Give the position of each P. falciparum parasite with its life-cycle stage, each leukocyte, and any debris.
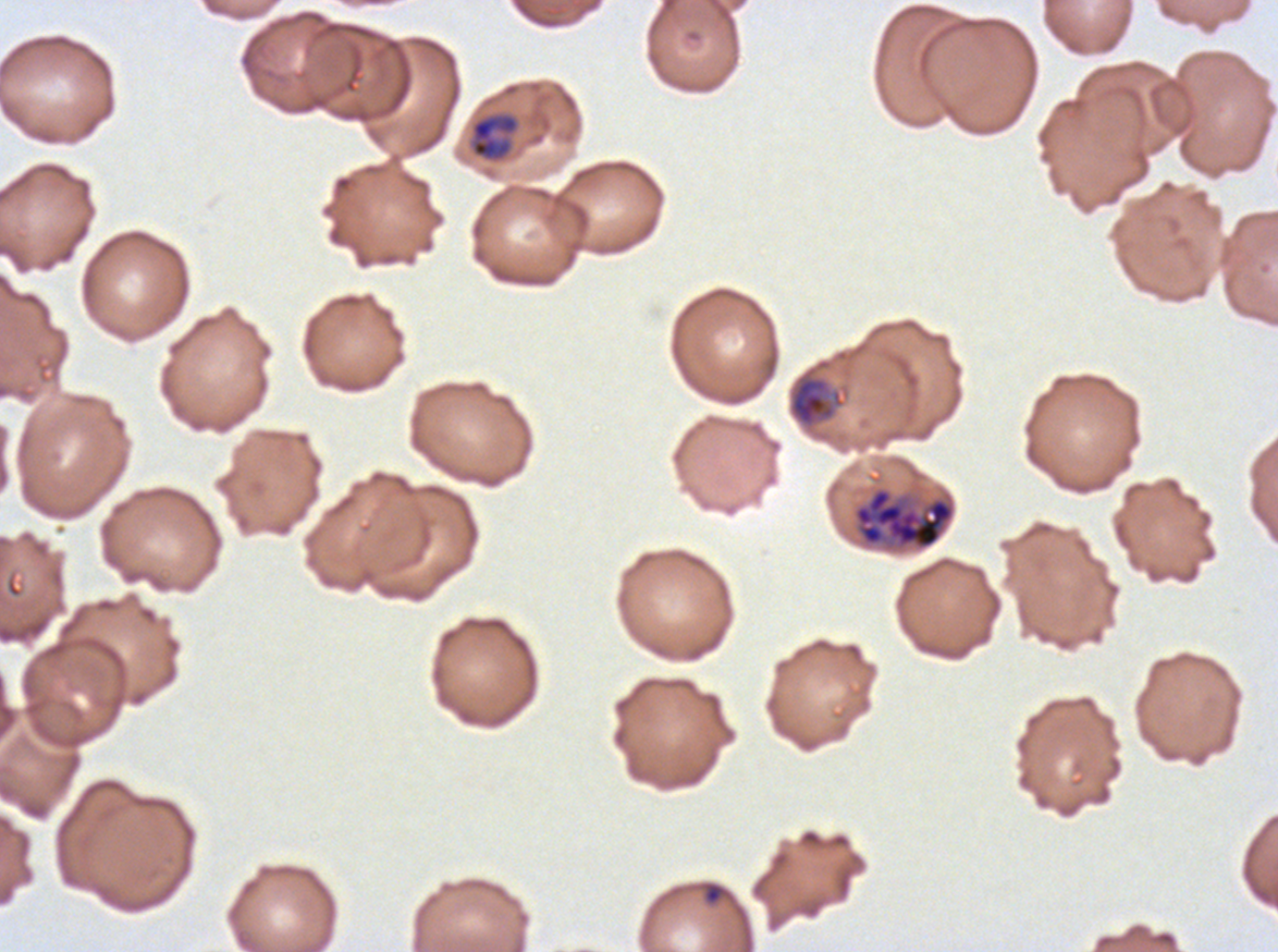
Approximate bounding boxes as [x1, y1, x2, y2] in pixels.
Rings: [704, 883, 722, 904].
Mid trophozoites: [470, 111, 520, 163], [787, 357, 851, 433].
Late schizonts: [852, 486, 956, 552].
No late-ring/early-trophozoite forms, late trophozoites, early schizonts, segmenters, gametocytes, leukocytes, or debris observed.

stain = Giemsa
life-cycle stages observed = ring, mid trophozoite, late schizont
image size = 1278×952 pixels
field of view = one sub-image of a larger composite
preparation = thin blood smear
specimen = P. falciparum from a patient in The Gambia, cultured ex vivo for 24 to 48 hours